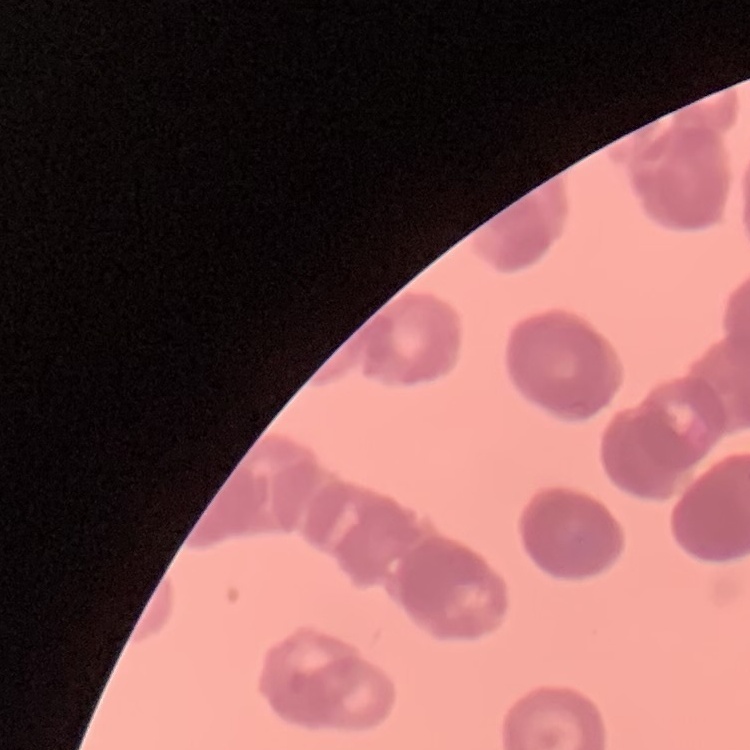
The red blood cells show rouleaux formation. Stained with either Field's or Giemsa. Thin blood film. Square crop of a larger photomicrograph.